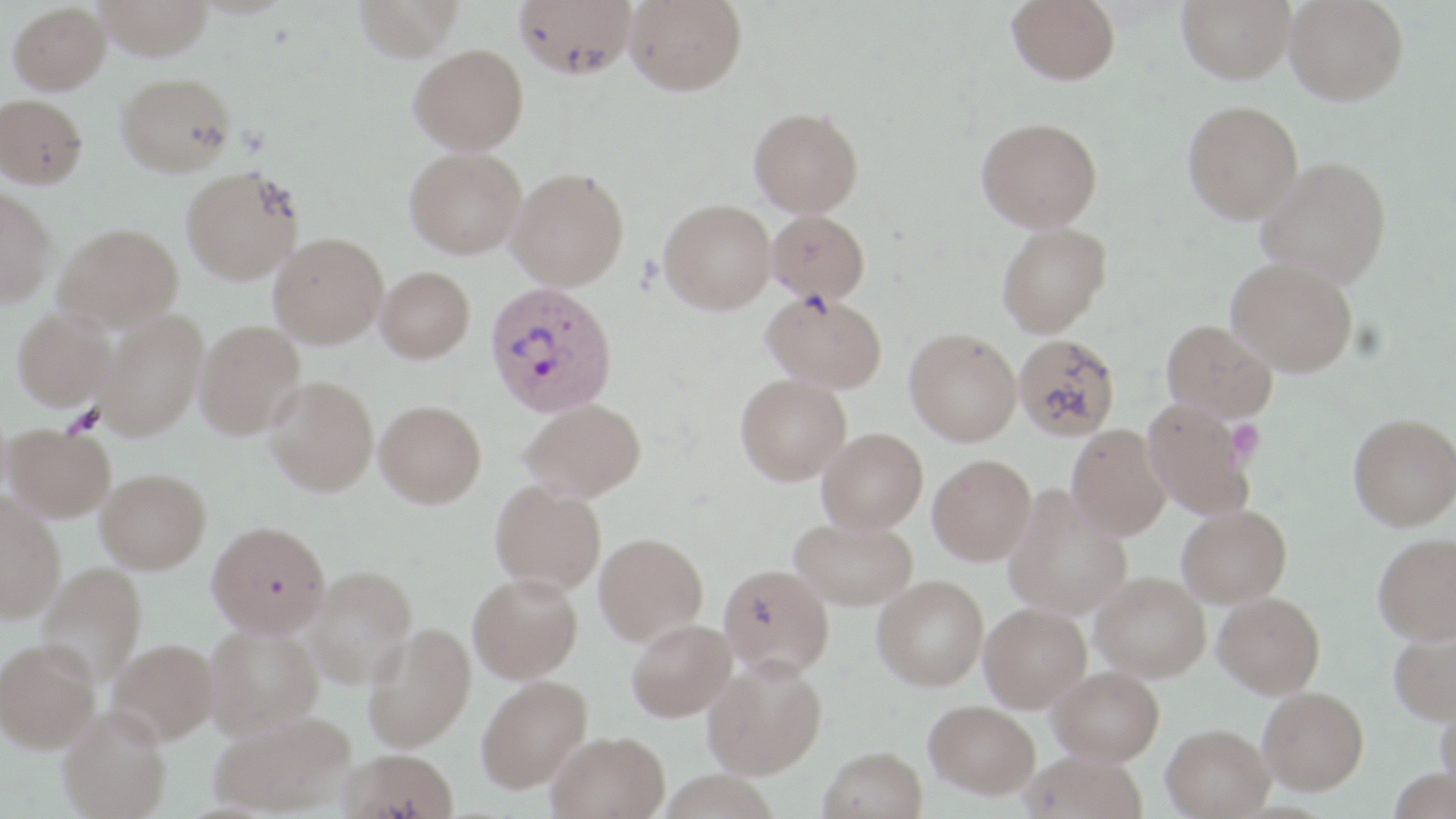

slide-level diagnosis = Plasmodium vivax
stain = May-Grünwald-Giemsa
field of view = single
Plasmodium vivax-infected red blood cell locations = approximate bounding boxes as (x1,y1)-(x2,y2) corner pairs in pixels: (485,281)-(618,417)
image size = 1456×819 pixels
preparation = thin blood film
modality = light microscopy
platelet locations = approximate bounding boxes as (x1,y1)-(x2,y2) corner pairs in pixels: (64,405)-(104,435), (1227,420)-(1265,464)
magnification = 1000x
uninfected red blood cell locations = approximate bounding boxes as (x1,y1)-(x2,y2) corner pairs in pixels: (96,0)-(214,60), (353,0)-(465,61), (514,0)-(637,79), (625,0)-(746,94), (1007,0)-(1120,85), (1177,0)-(1296,83), (1284,0)-(1408,105), (9,3)-(111,94), (409,43)-(528,154), (116,72)-(236,176), (0,94)-(88,188), (1182,100)-(1303,223), (749,106)-(863,217), (976,117)-(1102,232), (405,147)-(526,259), (1256,156)-(1392,288), (182,166)-(304,283), (507,167)-(629,290), (0,186)-(57,306), (659,199)-(776,314), (767,209)-(870,304), (997,222)-(1112,337), (55,223)-(183,330), (269,232)-(388,348), (1227,255)-(1359,376), (376,266)-(474,362), (763,291)-(887,392), (12,306)-(117,409), (95,309)-(208,440), (1162,320)-(1277,422), (195,321)-(305,438), (905,327)-(1021,445), (1013,334)-(1121,441), (736,374)-(851,484), (265,376)-(379,495), (522,398)-(645,501), (1142,398)-(1254,520), (375,400)-(486,507), (1348,412)-(1456,530), (5,423)-(115,521), (1067,425)-(1170,540), (817,428)-(927,534), (928,454)-(1037,565), (96,468)-(211,573), (491,481)-(606,594), (1004,486)-(1132,619), (0,494)-(65,622), (1177,505)-(1291,608), (790,517)-(917,610), (207,520)-(330,636), (1373,532)-(1456,644), (594,533)-(707,645), (39,561)-(147,684), (719,564)-(834,679), (305,565)-(418,687), (468,572)-(583,683), (1091,572)-(1210,682), (873,575)-(988,690), (1213,592)-(1325,697), (980,602)-(1092,711), (627,618)-(736,721), (364,623)-(475,752), (1388,623)-(1456,726), (204,624)-(322,737), (108,638)-(219,744), (1,640)-(100,752), (703,657)-(827,778), (1048,666)-(1164,765), (476,675)-(592,793), (1258,687)-(1369,794), (1436,697)-(1456,796), (925,700)-(1040,798), (58,706)-(171,819), (211,711)-(356,816), (1162,723)-(1275,818), (547,731)-(670,819), (819,746)-(928,819), (339,748)-(459,819), (1020,751)-(1148,819), (1388,767)-(1455,819)